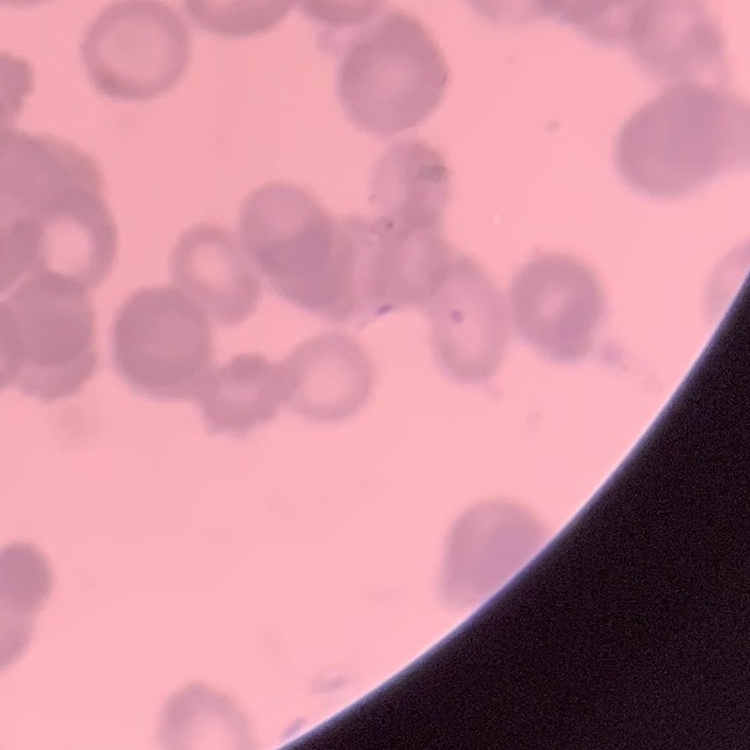 The red blood cells exhibit rouleaux formation. Thin blood smear. Stained with either Field's or Giemsa. One tile cut from a larger photomicrograph.